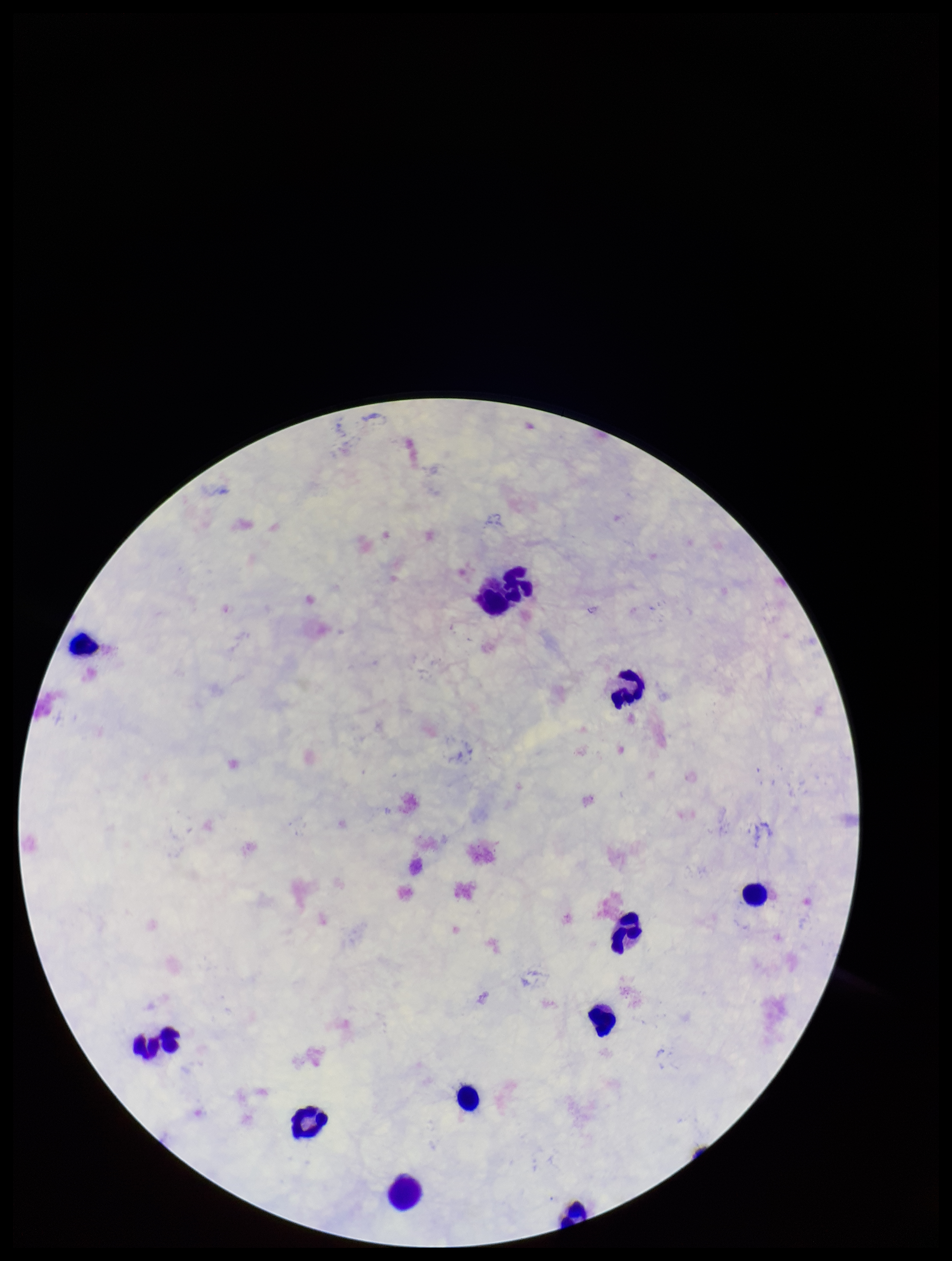
Summary:
  - Preparation: thick blood smear
  - Stain: Giemsa
  - Capture: smartphone photograph through the microscope eyepiece
  - Leukocyte count: 11
  - Image size: 952×1261 pixels
  - Plasmodium parasites: none identified
  - Parasite count: 0
  - Field of view: one from this slide
  - Patient malaria status: negative